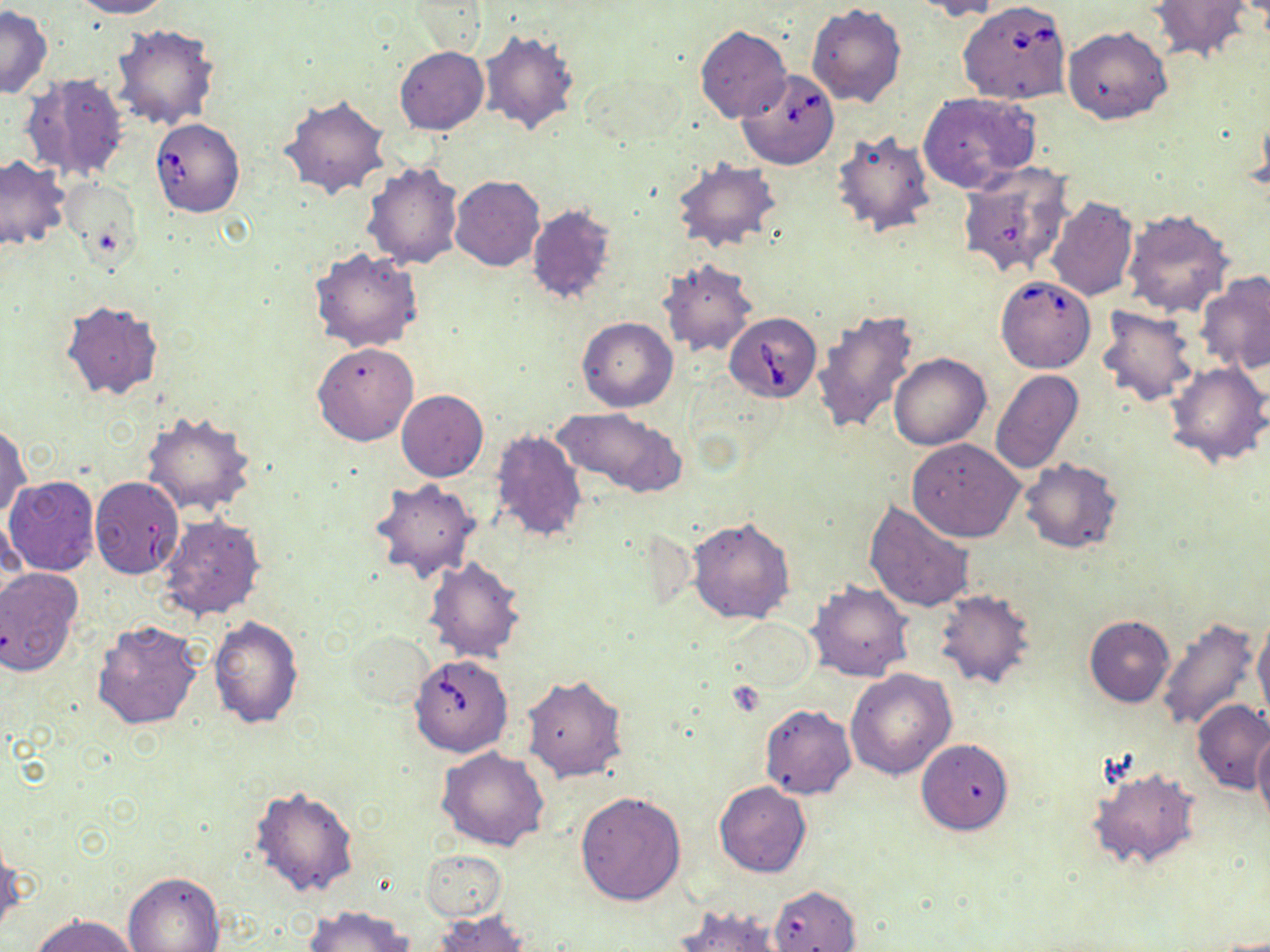

slide-level diagnosis = Babesia divergens
stain = May-Grünwald-Giemsa
image size = 1270×952 pixels
preparation = thin blood smear
magnification = 1000x
field of view = one of a larger specimen
Babesia divergens-infected red blood cell locations = approximate bounding boxes as [x1, y1, x2, y2] in pixels: [958, 1, 1072, 105], [737, 68, 840, 169], [149, 117, 246, 217], [995, 274, 1096, 373], [725, 311, 821, 403], [409, 654, 513, 756]
uninfected red blood cell locations = approximate bounding boxes as [x1, y1, x2, y2] in pixels: [69, 0, 171, 19], [913, 0, 1006, 21], [1151, 2, 1251, 62], [806, 4, 907, 108], [0, 7, 52, 99], [111, 23, 220, 130], [695, 25, 791, 123], [1063, 26, 1172, 125], [480, 29, 580, 136], [394, 47, 488, 135], [21, 72, 129, 182], [918, 92, 1040, 193], [280, 93, 390, 200], [830, 127, 936, 238], [0, 156, 68, 251], [671, 158, 780, 253], [362, 160, 464, 270], [956, 162, 1073, 279], [450, 176, 544, 273], [1045, 197, 1138, 302], [525, 205, 618, 306], [1123, 209, 1234, 318], [309, 246, 424, 353], [655, 258, 760, 360], [1196, 272, 1270, 374], [59, 299, 164, 400], [1096, 305, 1204, 409], [811, 306, 922, 438], [577, 316, 678, 411], [313, 342, 418, 446], [890, 354, 991, 450], [1164, 361, 1270, 469], [991, 369, 1084, 474], [396, 390, 488, 481], [555, 407, 685, 497], [139, 410, 257, 519], [0, 422, 32, 520], [490, 429, 587, 542], [908, 438, 1025, 542], [1018, 459, 1123, 554], [3, 474, 100, 577], [88, 477, 184, 579], [370, 480, 481, 583], [863, 499, 976, 614], [160, 515, 266, 620], [688, 517, 796, 624], [424, 556, 525, 664], [0, 568, 84, 678], [807, 581, 914, 682], [934, 589, 1039, 692], [209, 615, 305, 728], [1084, 615, 1176, 708], [1156, 615, 1260, 734], [722, 617, 816, 697], [92, 619, 203, 731], [1253, 619, 1270, 721], [347, 630, 436, 709], [845, 668, 956, 780], [521, 674, 627, 783], [1192, 700, 1270, 795], [759, 704, 856, 798], [1253, 727, 1270, 832], [916, 739, 1014, 834], [438, 746, 551, 851], [1087, 765, 1202, 871], [714, 781, 811, 877], [248, 785, 360, 898], [574, 790, 686, 906], [0, 833, 24, 936], [422, 848, 508, 921], [123, 872, 225, 952], [768, 884, 861, 952], [302, 905, 414, 952], [670, 905, 793, 951], [432, 911, 530, 952], [31, 913, 142, 952]
modality = light microscopy